Assess this cell for malaria.
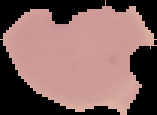
Uninfected.

Summary:
  - Image type: cell region segmented out of the field of view; surrounding area masked to black
  - Image size: 157×115 pixels
  - Preparation: thin blood smear